Report the malaria status of this cell.
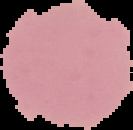

It is uninfected.

From a thin blood smear. Image is 133×130 pixels. Cell region segmented out of the field of view; the surrounding area is masked to black.